Outline every leukocyte.
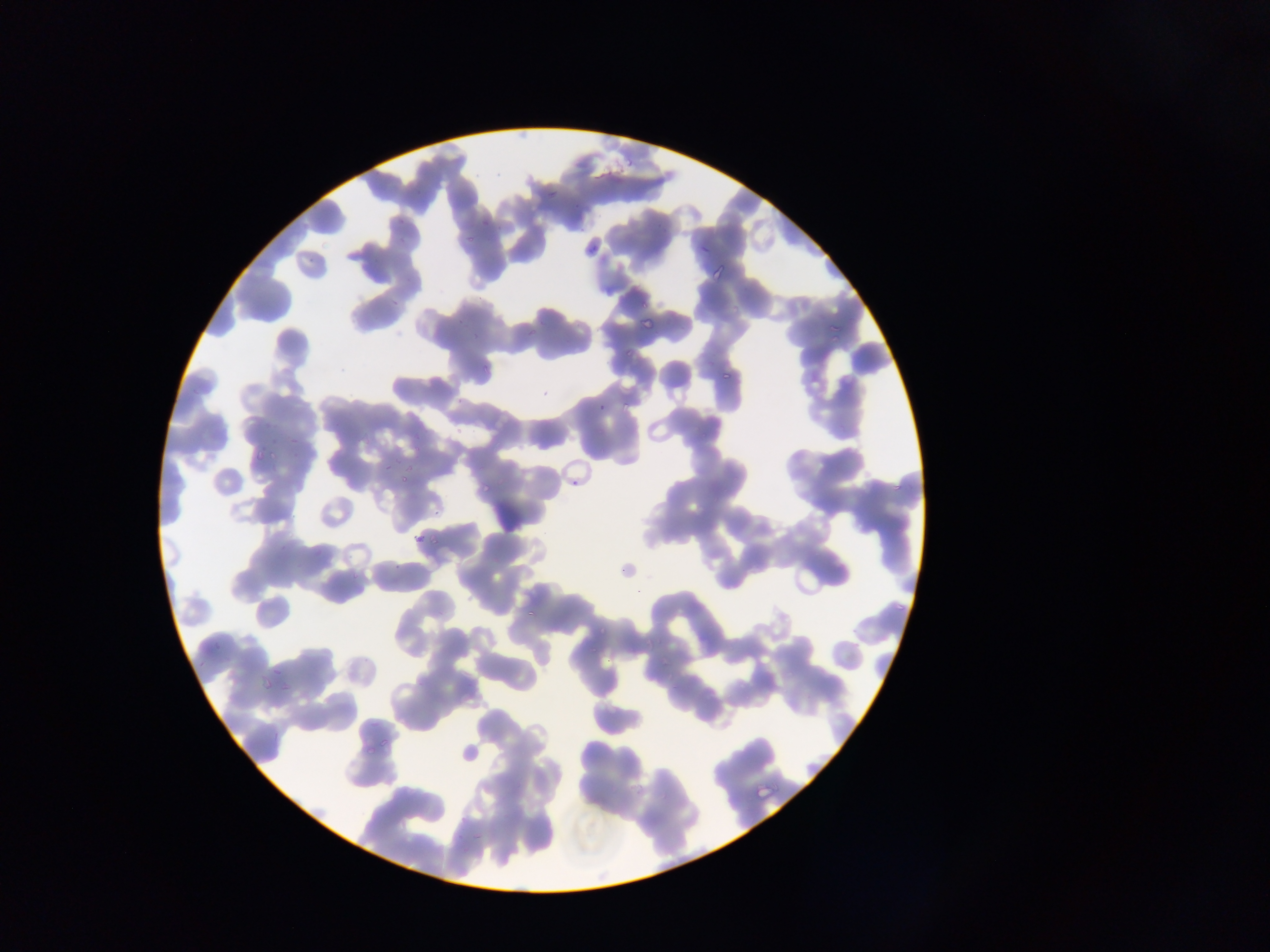

No leukocytes observed.

{
  "preparation": "thin blood film",
  "image_size": "1270×952 pixels",
  "country": "Ghana",
  "capture": "mobile-phone photograph through a microscope",
  "malaria_parasite_locations": "approximate bounding boxes as left top right bottom in pixels: 623 153 635 168; 593 168 611 180; 544 187 559 203; 393 216 406 228; 462 233 477 249; 584 241 605 258; 709 262 729 281; 389 296 403 306; 729 304 745 313; 635 315 659 332; 826 320 843 337; 522 323 542 345; 621 346 636 361; 479 362 495 381; 717 367 737 386; 617 401 633 417; 596 403 606 411; 287 434 302 451; 254 450 271 469; 381 460 395 473; 400 472 412 484; 570 476 580 487; 477 480 493 498; 890 481 906 497; 413 533 431 549; 523 600 542 623; 893 601 907 614; 596 623 613 637; 657 657 671 667; 261 672 275 692; 378 734 395 753; 457 739 483 769; 753 779 780 805",
  "field_of_view": "single"
}